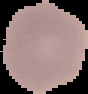

Summary:
  - Image type: segmented cell region on a black background
  - Preparation: thin blood smear
  - Result: negative for malaria parasites
  - Image size: 88×94 pixels